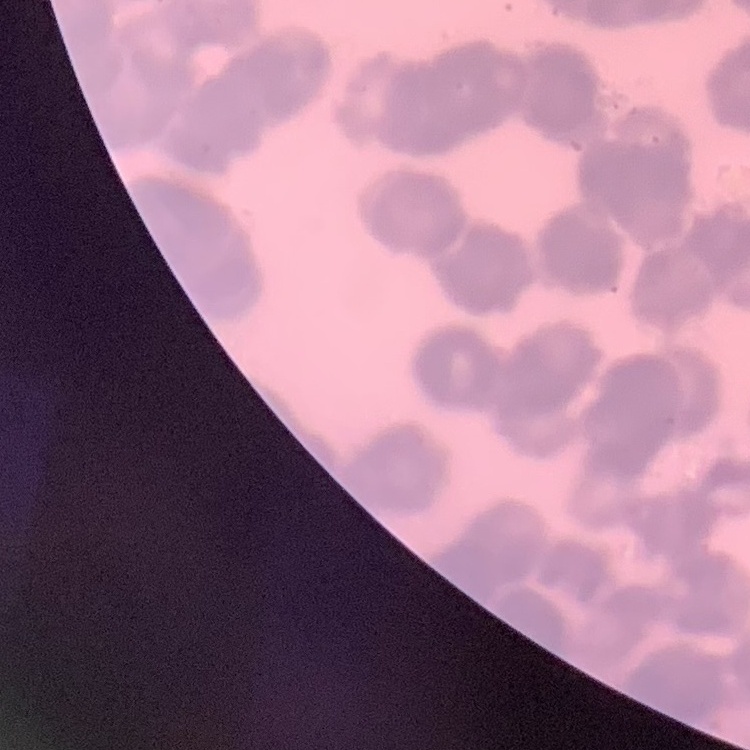
red blood cell morphology = rouleaux formation
preparation = thin peripheral smear
stain = Field's or Giemsa
image type = one tile cut from a larger photomicrograph